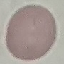

Malaria status: uninfected. Cell patch, automatically extracted from a larger field of view and resized to 64 × 64 pixels. Thin blood film. Acquired by smartphone through the microscope eyepiece. Giemsa stain.